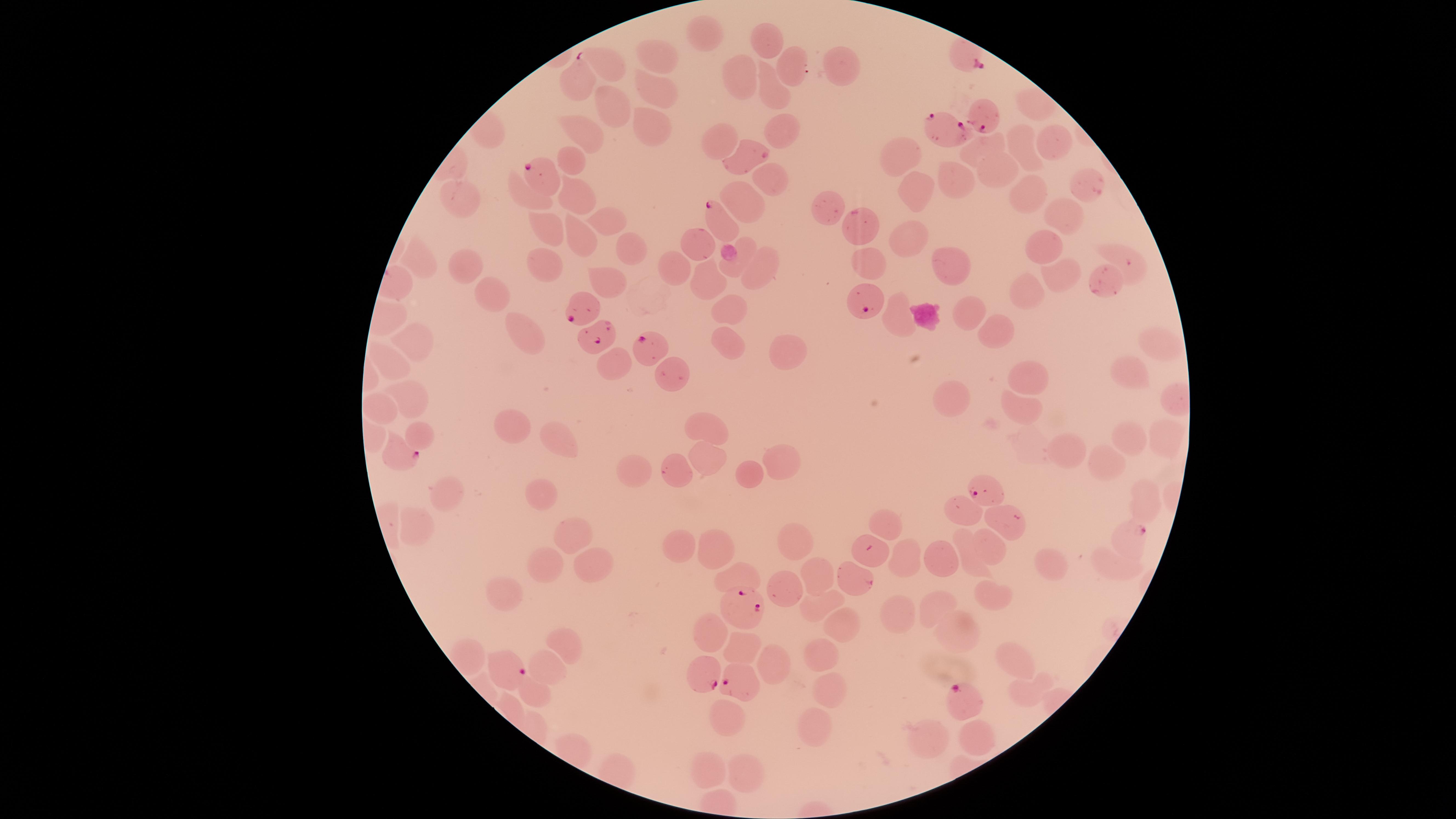
Approximate marker points as [x, y] in pixels.
Summary:
  - Parasitized red blood cells: [577, 80], [986, 117], [950, 130], [547, 175], [718, 220], [866, 294], [581, 309], [592, 336], [649, 345], [396, 455], [981, 490], [1127, 534], [746, 608], [506, 668], [703, 675], [740, 682], [961, 699]
  - Uninfected red blood cells: [703, 33], [768, 37], [660, 59], [793, 66], [834, 67], [608, 68], [743, 78], [652, 88], [769, 94], [608, 104], [1031, 106], [647, 125], [783, 129], [584, 131], [724, 136], [1054, 140], [1021, 147], [980, 148], [754, 149], [905, 153], [573, 154], [999, 169], [770, 177], [956, 177], [1082, 183], [1029, 187], [916, 190], [574, 193], [524, 195], [461, 200], [745, 203], [828, 204], [1066, 215], [603, 216], [548, 222], [867, 224], [913, 234], [580, 236], [699, 240], [1049, 243], [627, 246], [1125, 260], [424, 261], [543, 261], [868, 261], [464, 262], [951, 262], [673, 263], [734, 267], [759, 267], [1059, 277], [1106, 278], [711, 279], [602, 281], [490, 289], [1027, 291], [724, 310], [971, 311], [897, 315], [1001, 325], [526, 332], [726, 337], [1151, 340], [416, 341], [775, 350], [390, 360], [610, 361], [1128, 369], [670, 373], [1030, 374], [408, 392], [955, 395], [381, 402], [1025, 410], [519, 424], [710, 429], [424, 434], [1128, 434], [1167, 438], [560, 441], [1069, 446], [706, 457], [1107, 463], [781, 464], [673, 469], [631, 474], [752, 476], [450, 488], [541, 494], [1142, 500], [964, 509], [885, 514], [1009, 520], [417, 526], [570, 530], [805, 543], [677, 544], [990, 547], [713, 553], [901, 553], [942, 553], [874, 556], [971, 558], [1054, 562], [592, 564], [1110, 564], [544, 567], [819, 571], [746, 573], [849, 573], [786, 582], [502, 588], [990, 591], [936, 602], [819, 604], [906, 613], [841, 624], [709, 628], [958, 628], [568, 643], [748, 647], [819, 657], [772, 661], [1014, 661], [546, 665], [535, 686], [1030, 691], [830, 693], [721, 721], [816, 721], [925, 738], [976, 739], [706, 758], [744, 767]
  - Image size: 1456×819 pixels
  - Field of view: single
  - Preparation: thin blood film
  - Species: Plasmodium falciparum
  - Presence: malaria parasites detected
  - Capture: smartphone photograph through the microscope eyepiece
  - Visible region: circular
  - Stain: Giemsa